State the blood parasite species.
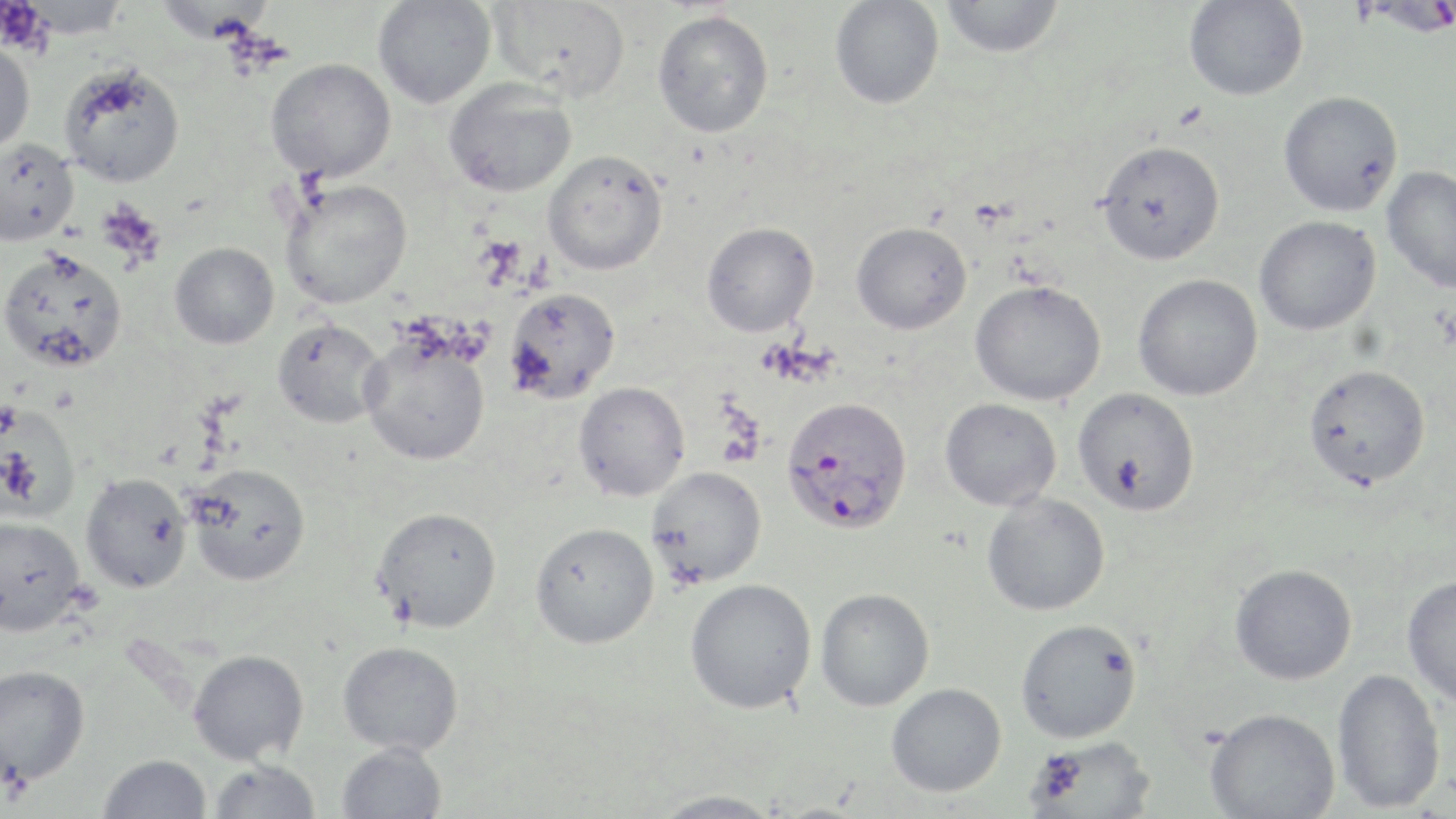
Plasmodium falciparum.

Approximate bounding boxes as named x1/y1/x2/y2 corners in pixels. Uninfected red blood cell locations: (x1=22, y1=0, x2=129, y2=39), (x1=372, y1=0, x2=496, y2=109), (x1=489, y1=0, x2=632, y2=101), (x1=939, y1=0, x2=1064, y2=58), (x1=829, y1=1, x2=944, y2=109), (x1=1183, y1=1, x2=1308, y2=101), (x1=652, y1=10, x2=774, y2=138), (x1=0, y1=41, x2=35, y2=158), (x1=266, y1=57, x2=396, y2=182), (x1=59, y1=63, x2=185, y2=187), (x1=444, y1=79, x2=576, y2=197), (x1=1278, y1=91, x2=1403, y2=217), (x1=1, y1=139, x2=79, y2=246), (x1=1096, y1=140, x2=1225, y2=265), (x1=542, y1=149, x2=668, y2=275), (x1=1382, y1=166, x2=1456, y2=294), (x1=280, y1=178, x2=412, y2=309), (x1=1254, y1=216, x2=1380, y2=336), (x1=701, y1=221, x2=819, y2=337), (x1=851, y1=222, x2=972, y2=335), (x1=169, y1=242, x2=279, y2=349), (x1=0, y1=248, x2=128, y2=372), (x1=1132, y1=274, x2=1263, y2=401), (x1=969, y1=280, x2=1106, y2=406), (x1=504, y1=287, x2=620, y2=405), (x1=272, y1=318, x2=387, y2=429), (x1=359, y1=334, x2=490, y2=465), (x1=1304, y1=364, x2=1431, y2=489), (x1=573, y1=381, x2=690, y2=501), (x1=1072, y1=387, x2=1200, y2=516), (x1=940, y1=398, x2=1062, y2=511), (x1=1, y1=404, x2=81, y2=522), (x1=186, y1=462, x2=311, y2=586), (x1=646, y1=466, x2=767, y2=587), (x1=81, y1=473, x2=192, y2=593), (x1=981, y1=492, x2=1110, y2=616), (x1=373, y1=506, x2=502, y2=632), (x1=0, y1=516, x2=85, y2=635), (x1=530, y1=522, x2=659, y2=649), (x1=1229, y1=563, x2=1357, y2=685), (x1=1402, y1=575, x2=1456, y2=707), (x1=685, y1=578, x2=817, y2=714), (x1=816, y1=588, x2=935, y2=711), (x1=1015, y1=618, x2=1142, y2=743), (x1=337, y1=640, x2=463, y2=754), (x1=188, y1=649, x2=309, y2=765), (x1=0, y1=665, x2=90, y2=784), (x1=1331, y1=668, x2=1446, y2=814), (x1=885, y1=683, x2=1007, y2=797), (x1=1205, y1=707, x2=1340, y2=819), (x1=1025, y1=736, x2=1156, y2=818), (x1=337, y1=742, x2=447, y2=819), (x1=98, y1=753, x2=211, y2=818), (x1=208, y1=760, x2=321, y2=818), (x1=648, y1=789, x2=785, y2=818). Plasmodium falciparum-infected red blood cell locations: (x1=1355, y1=0, x2=1456, y2=36), (x1=780, y1=397, x2=914, y2=534). Platelet locations: (x1=0, y1=1, x2=49, y2=52). Single field of view. Captured at 1000x magnification. May-Grünwald-Giemsa stain. Thin blood film. Image is 1456×819 pixels. Light microscopy.